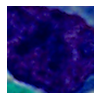 Photomicrograph. Captured at 1000x magnification. A white blood cell is shown.